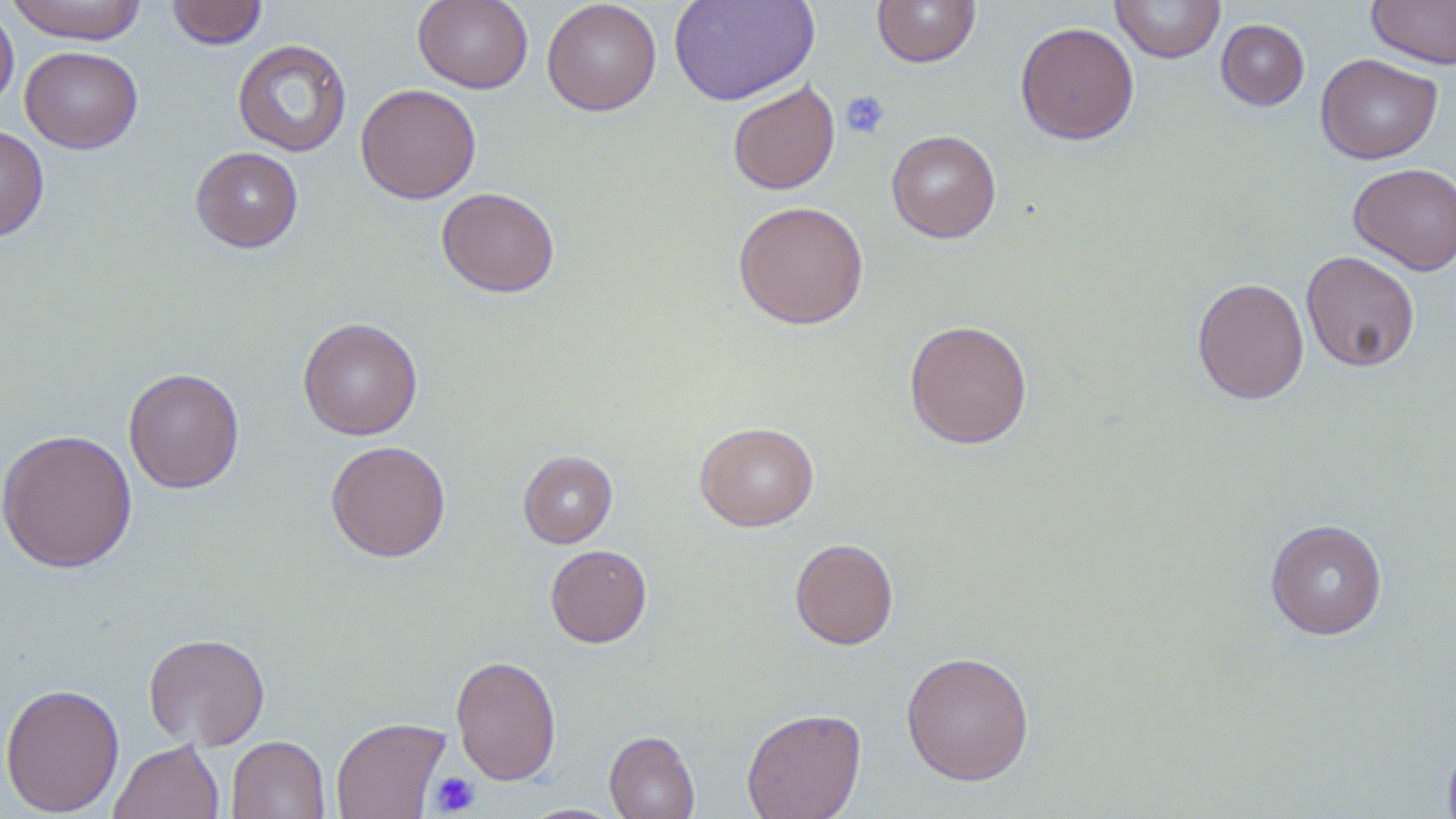
{
  "slide_level_diagnosis": "no evidence of blood parasites",
  "image_size": "1456×819 pixels",
  "field_of_view": "single",
  "preparation": "thin blood film",
  "stain": "May-Grünwald-Giemsa",
  "magnification": "1000x",
  "uninfected_red_blood_cell_locations": "approximate bounding boxes as named x1/y1/x2/y2 corners in pixels: (x1=7, y1=0, x2=147, y2=44), (x1=166, y1=0, x2=268, y2=49), (x1=412, y1=0, x2=534, y2=93), (x1=542, y1=0, x2=662, y2=116), (x1=668, y1=0, x2=820, y2=106), (x1=871, y1=0, x2=981, y2=67), (x1=1366, y1=0, x2=1456, y2=68), (x1=1110, y1=1, x2=1226, y2=63), (x1=0, y1=4, x2=19, y2=116), (x1=1215, y1=18, x2=1309, y2=110), (x1=1014, y1=22, x2=1140, y2=144), (x1=232, y1=39, x2=352, y2=157), (x1=20, y1=46, x2=143, y2=153), (x1=1315, y1=53, x2=1442, y2=164), (x1=727, y1=80, x2=840, y2=195), (x1=355, y1=83, x2=481, y2=204), (x1=0, y1=123, x2=49, y2=243), (x1=886, y1=130, x2=1001, y2=243), (x1=190, y1=147, x2=304, y2=253), (x1=1348, y1=162, x2=1456, y2=275), (x1=436, y1=187, x2=560, y2=297), (x1=733, y1=200, x2=869, y2=329), (x1=1300, y1=250, x2=1420, y2=372), (x1=1191, y1=276, x2=1309, y2=404), (x1=297, y1=317, x2=422, y2=440), (x1=904, y1=319, x2=1033, y2=449), (x1=123, y1=367, x2=245, y2=494), (x1=694, y1=421, x2=819, y2=532), (x1=0, y1=428, x2=138, y2=573), (x1=325, y1=440, x2=452, y2=562), (x1=518, y1=450, x2=618, y2=548), (x1=1265, y1=518, x2=1388, y2=640), (x1=789, y1=538, x2=899, y2=650), (x1=545, y1=544, x2=652, y2=648), (x1=143, y1=632, x2=270, y2=750), (x1=901, y1=650, x2=1035, y2=786), (x1=450, y1=655, x2=562, y2=785), (x1=0, y1=682, x2=125, y2=817), (x1=742, y1=708, x2=866, y2=818), (x1=330, y1=716, x2=450, y2=819), (x1=604, y1=731, x2=700, y2=819), (x1=1442, y1=733, x2=1456, y2=819), (x1=226, y1=735, x2=330, y2=819), (x1=109, y1=739, x2=225, y2=819)",
  "modality": "optical microscopy",
  "platelet_locations": "approximate bounding boxes as named x1/y1/x2/y2 corners in pixels: (x1=840, y1=91, x2=890, y2=140), (x1=429, y1=771, x2=481, y2=816)"
}